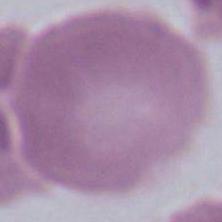 Micrograph. A red blood cell is seen. 1000x magnification.